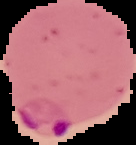
Summary:
  - Image size: 136×145 pixels
  - Preparation: thin blood smear
  - Malaria status: parasitized
  - Image type: cell region segmented out of the field of view; surrounding area masked to black